Describe the morphology of the red blood cells.
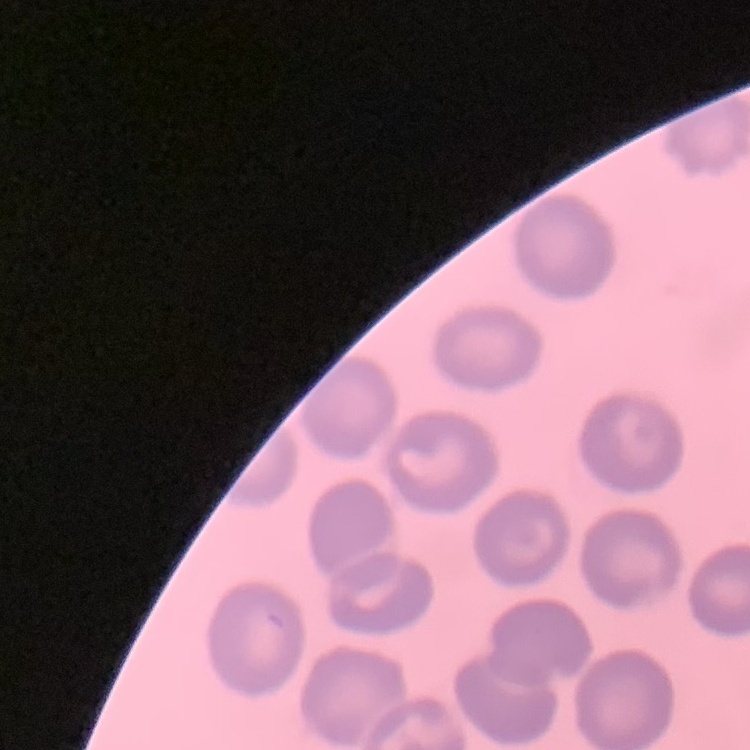

No rouleaux formation.

Thin blood smear. Square crop of a larger photomicrograph. Field's or Giemsa stain.